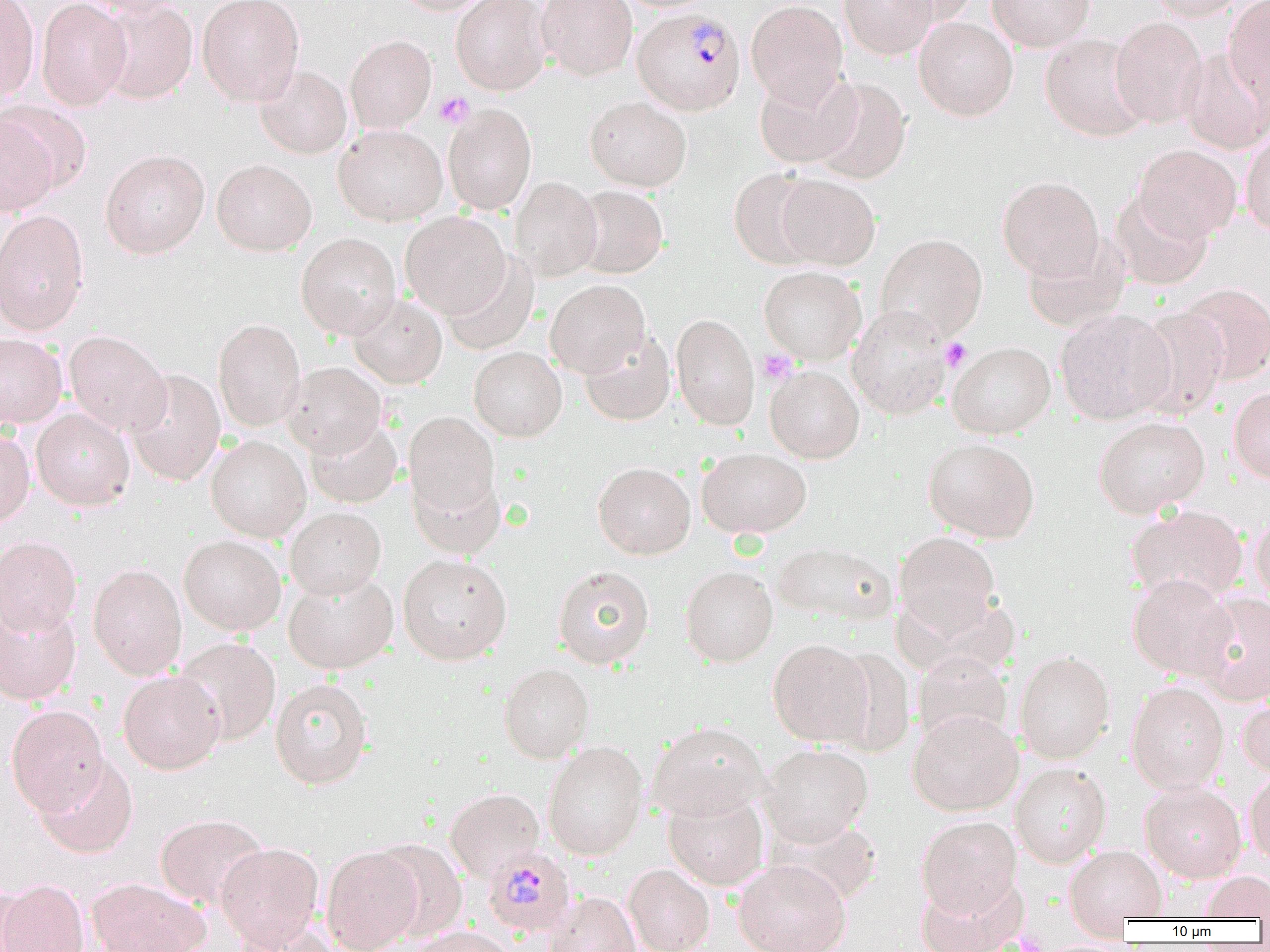
Approximate bounding boxes as [x1, y1, x2, y2] in pixels. Plasmodium malariae-infected red blood cell locations: [632, 7, 746, 115], [482, 846, 576, 937]. Platelet locations: [435, 92, 474, 128], [940, 337, 972, 371], [758, 349, 796, 384]. Uninfected red blood cell locations: [0, 0, 40, 101], [35, 0, 132, 111], [76, 0, 189, 17], [95, 0, 197, 103], [197, 0, 304, 105], [392, 0, 492, 15], [451, 0, 551, 95], [536, 0, 638, 80], [745, 0, 849, 106], [839, 0, 937, 59], [884, 0, 981, 25], [987, 0, 1094, 51], [1144, 0, 1249, 21], [1223, 0, 1270, 107], [913, 16, 1018, 121], [1110, 16, 1208, 128], [1040, 33, 1150, 141], [345, 35, 436, 133], [1180, 48, 1270, 154], [254, 65, 352, 159], [754, 70, 860, 168], [808, 77, 912, 184], [585, 96, 692, 191], [443, 104, 537, 215], [0, 113, 59, 217], [333, 123, 447, 226], [1241, 130, 1270, 235], [1133, 144, 1242, 243], [100, 149, 210, 258], [211, 159, 316, 256], [728, 168, 824, 269], [775, 173, 881, 270], [510, 176, 602, 281], [997, 176, 1104, 281], [572, 185, 668, 278], [1110, 190, 1214, 290], [0, 209, 90, 336], [400, 212, 511, 319], [295, 233, 401, 338], [875, 233, 988, 341], [1022, 236, 1130, 333], [442, 254, 539, 355], [759, 265, 867, 364], [545, 279, 650, 378], [1177, 283, 1270, 384], [348, 293, 448, 388], [847, 305, 953, 420], [1131, 307, 1230, 420], [1055, 309, 1175, 425], [670, 314, 760, 430], [213, 318, 306, 432], [64, 330, 171, 436], [580, 330, 676, 426], [0, 333, 67, 428], [947, 341, 1056, 438], [469, 346, 567, 441], [282, 362, 387, 458], [765, 365, 864, 463], [124, 368, 225, 486], [1229, 386, 1270, 485], [31, 407, 135, 510], [403, 411, 501, 524], [1093, 416, 1210, 518], [305, 417, 403, 508], [0, 429, 35, 529], [206, 435, 311, 542], [923, 437, 1040, 542], [697, 447, 812, 539], [593, 462, 696, 559], [408, 466, 505, 560], [1127, 505, 1248, 604], [285, 507, 386, 600], [1250, 513, 1270, 609], [893, 532, 1001, 639], [179, 535, 286, 636], [0, 537, 83, 636], [772, 541, 898, 626], [398, 553, 512, 665], [88, 564, 187, 680], [552, 565, 655, 669], [680, 566, 778, 666], [283, 572, 398, 674], [1128, 574, 1237, 680], [1191, 592, 1270, 704], [0, 598, 82, 705], [173, 637, 281, 746], [767, 639, 875, 747], [1014, 649, 1115, 764], [911, 652, 1014, 747], [498, 663, 594, 762], [118, 670, 225, 774], [270, 678, 373, 789], [1126, 681, 1229, 792], [1237, 691, 1270, 779], [6, 705, 109, 816], [908, 709, 1023, 815], [648, 722, 770, 820], [543, 741, 649, 859], [759, 743, 874, 846], [34, 755, 138, 859], [1009, 763, 1112, 868], [1244, 770, 1270, 865], [1140, 782, 1247, 882], [445, 788, 545, 882], [663, 789, 769, 890], [155, 813, 268, 910], [767, 814, 884, 906], [917, 816, 1022, 918], [372, 839, 467, 942], [215, 842, 324, 950], [1064, 845, 1167, 926], [321, 846, 424, 952], [733, 859, 851, 952], [623, 863, 715, 952], [1198, 871, 1270, 920], [86, 877, 210, 952], [0, 879, 90, 952], [915, 879, 1024, 952], [0, 884, 33, 952], [544, 891, 642, 952], [230, 919, 341, 952], [408, 925, 518, 952]. Slide-level diagnosis: Plasmodium malariae. Single field of view. Image is 1270×952 pixels. 1000x magnification. Optical microscopy. Thin blood film.